Give the preparation type.
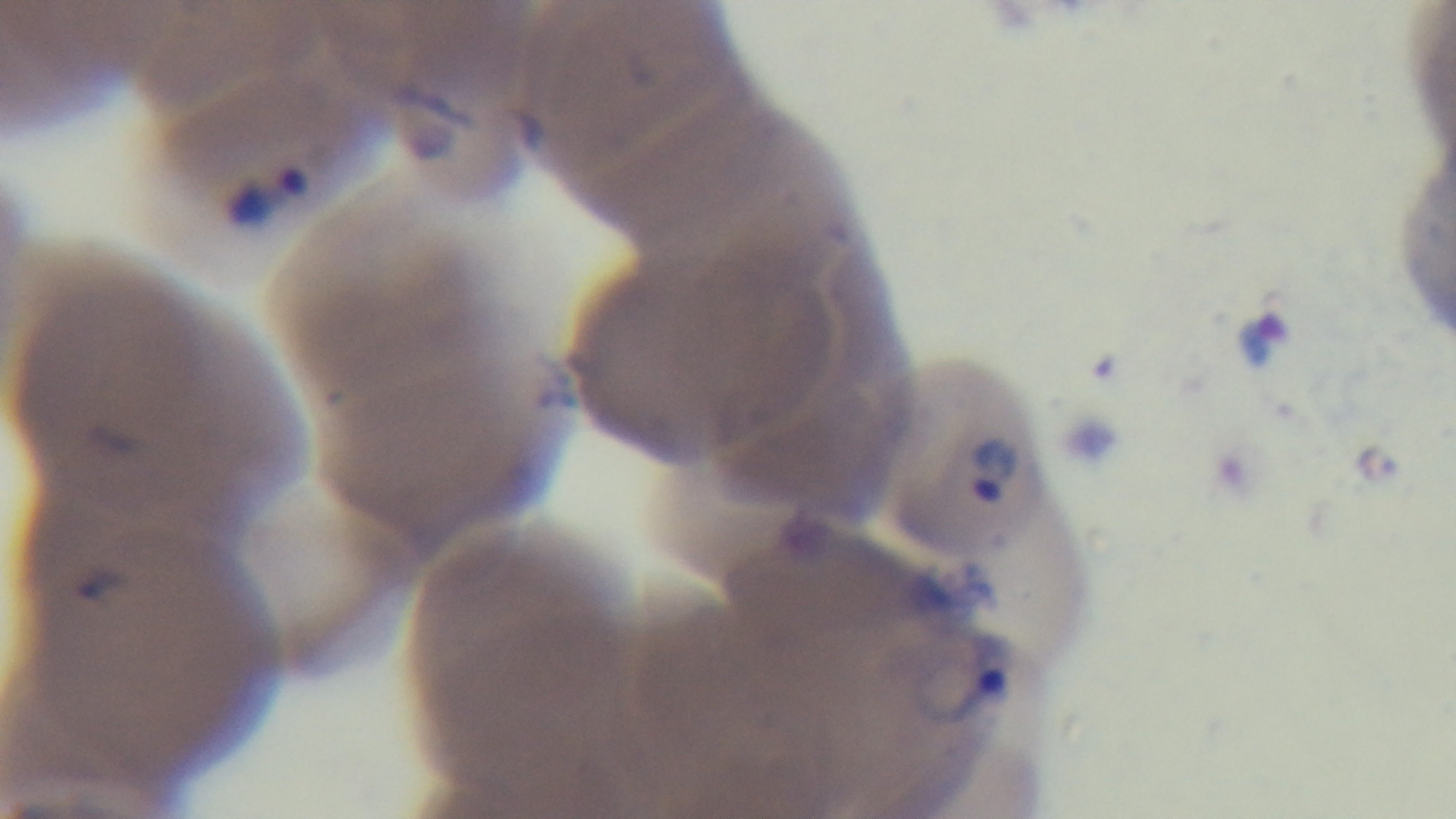
It is a thin blood film.

Summary:
  - Stain: Giemsa
  - Capture: mounted 4K digital camera
  - Malaria status: infected
  - Objective: 100x oil immersion
  - Field of view: single
  - Modality: light microscopy